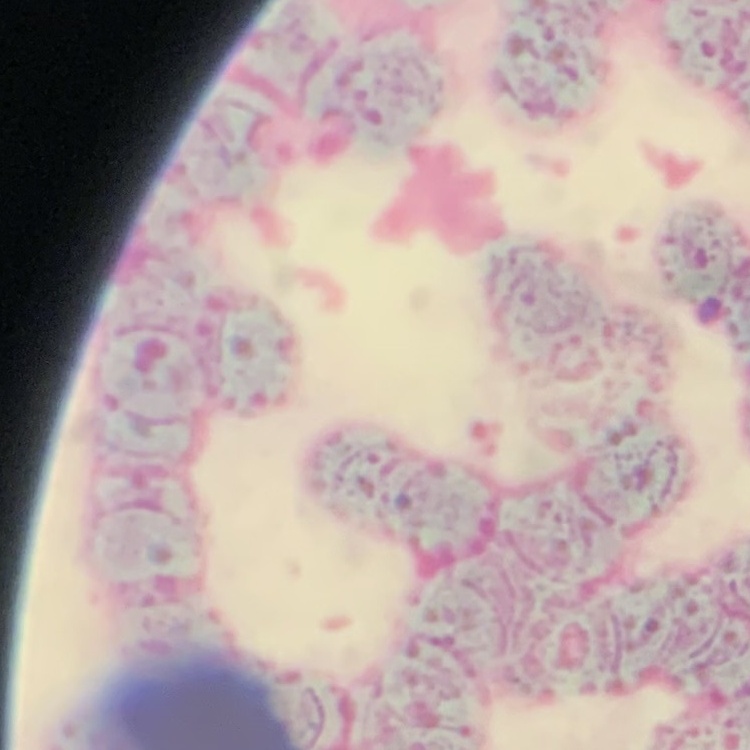
The erythrocytes exhibit rouleaux formation. Thin blood smear. Field's or Giemsa stain. Square crop of a larger photomicrograph.